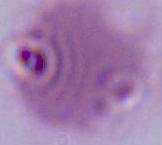
Captured at 1000x magnification. A red blood cell is shown. Photomicrograph.